State which cell type is depicted.
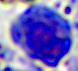
A leukocyte.

magnification: 400x
modality: micrograph